Outline platelets.
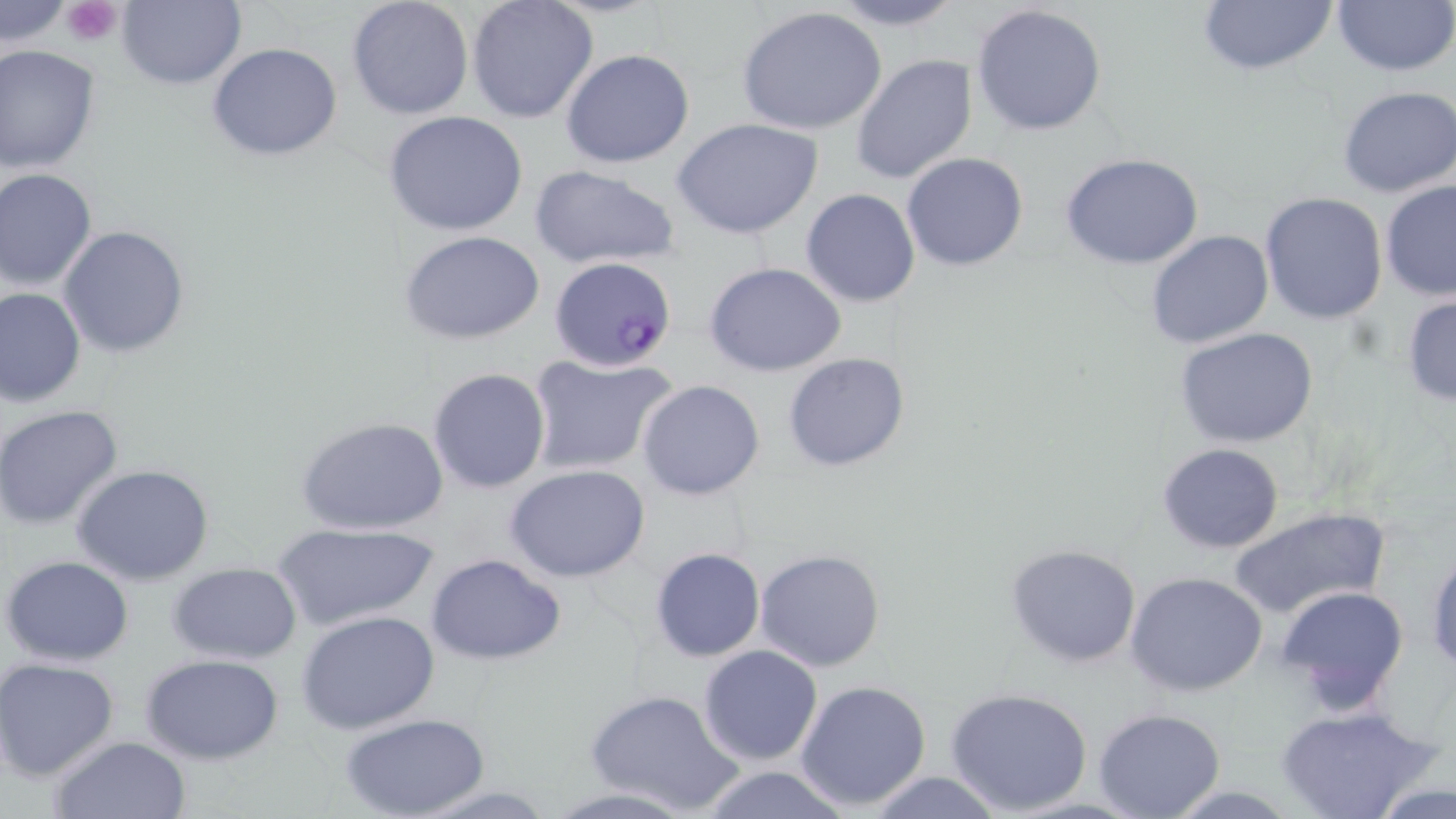
Approximate bounding boxes as (x1, y1, x2, y2) in pixels.
Platelets: (61, 0, 126, 44).

{
  "slide_level_diagnosis": "Plasmodium falciparum",
  "field_of_view": "one of a larger specimen",
  "uninfected_red_blood_cell_locations": "approximate bounding boxes as (x1, y1, x2, y2) in pixels: (346, 0, 474, 119), (466, 0, 599, 123), (822, 0, 971, 31), (1197, 0, 1337, 79), (1330, 0, 1455, 79), (117, 1, 243, 90), (0, 2, 74, 51), (971, 3, 1109, 137), (738, 7, 888, 137), (207, 42, 342, 161), (0, 45, 101, 174), (561, 48, 695, 168), (849, 53, 978, 186), (1336, 84, 1456, 198), (383, 110, 529, 237), (672, 119, 823, 240), (901, 151, 1029, 272), (1060, 152, 1205, 270), (530, 166, 678, 271), (0, 168, 98, 290), (1379, 179, 1456, 300), (800, 188, 921, 308), (1259, 192, 1388, 325), (59, 225, 188, 358), (400, 230, 547, 346), (1146, 230, 1274, 349), (703, 261, 848, 378), (1, 285, 86, 406), (1401, 292, 1456, 409), (1174, 327, 1320, 446), (525, 352, 679, 475), (783, 352, 912, 474), (427, 367, 551, 495), (637, 380, 765, 499), (0, 405, 125, 531), (298, 417, 448, 536), (1157, 442, 1285, 554), (72, 463, 217, 587), (506, 463, 651, 583), (1227, 505, 1393, 619), (271, 522, 439, 633), (1005, 542, 1143, 668), (649, 547, 764, 663), (1426, 547, 1456, 673), (755, 548, 886, 672), (427, 553, 566, 665), (2, 555, 134, 666), (169, 563, 302, 665), (1126, 569, 1269, 698), (1275, 584, 1409, 716), (296, 609, 442, 734), (697, 645, 823, 766), (141, 653, 285, 764), (0, 658, 120, 780), (793, 678, 934, 812), (946, 686, 1096, 816), (585, 688, 743, 815), (1277, 704, 1436, 819), (1092, 709, 1226, 819), (343, 714, 488, 819), (48, 735, 192, 819), (699, 765, 851, 819), (863, 771, 1004, 818), (410, 783, 559, 818), (540, 786, 704, 818)",
  "modality": "light microscopy",
  "preparation": "thin blood smear",
  "magnification": "1000x",
  "image_size": "1456×819 pixels",
  "stain": "May-Grünwald-Giemsa",
  "plasmodium_falciparum_infected_red_blood_cell_locations": "approximate bounding boxes as (x1, y1, x2, y2) in pixels: (548, 256, 678, 375)"
}